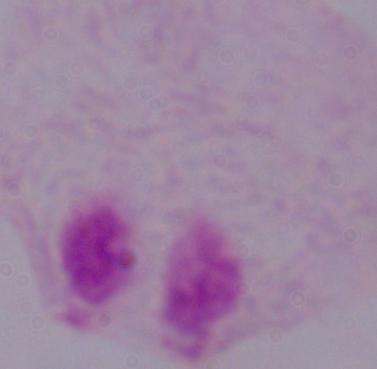

Photomicrograph. 1000x magnification. A trichomonad is seen.